Report the malaria status of this cell.
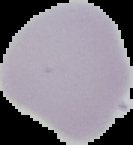

Uninfected.

image type = cell region segmented out of the field of view; surrounding area masked to black
preparation = thin blood smear
image size = 133×145 pixels